Name the cell type shown.
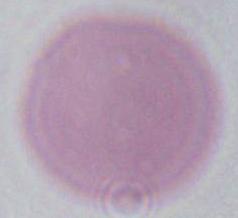
This is an erythrocyte.

modality = micrograph
magnification = 1000x